Report the malaria status of this cell.
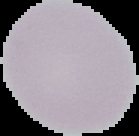
Uninfected.

Image is 139×136 pixels. Segmented cell region on a black background. From a thin blood film.